Give the preparation type.
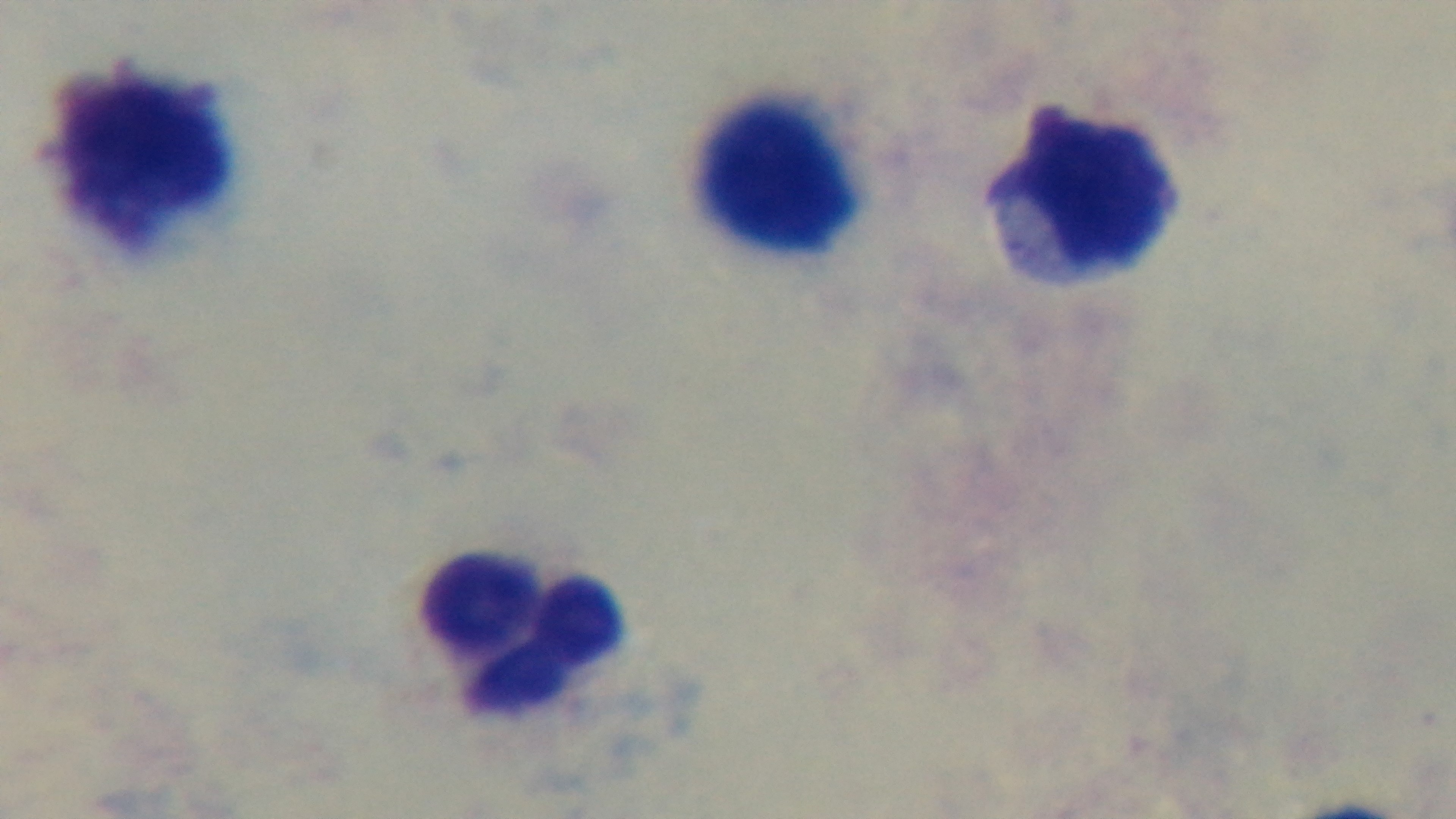
It is a thick blood film.

Summary:
  - Capture: mounted 4K digital camera
  - Stain: Giemsa
  - Field of view: one from the slide
  - Modality: light microscopy
  - Objective: 100x oil immersion
  - Malaria status: uninfected